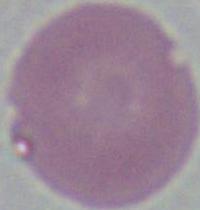
Summary:
  - Magnification: 1000x
  - Modality: photomicrograph
  - Identification: erythrocyte